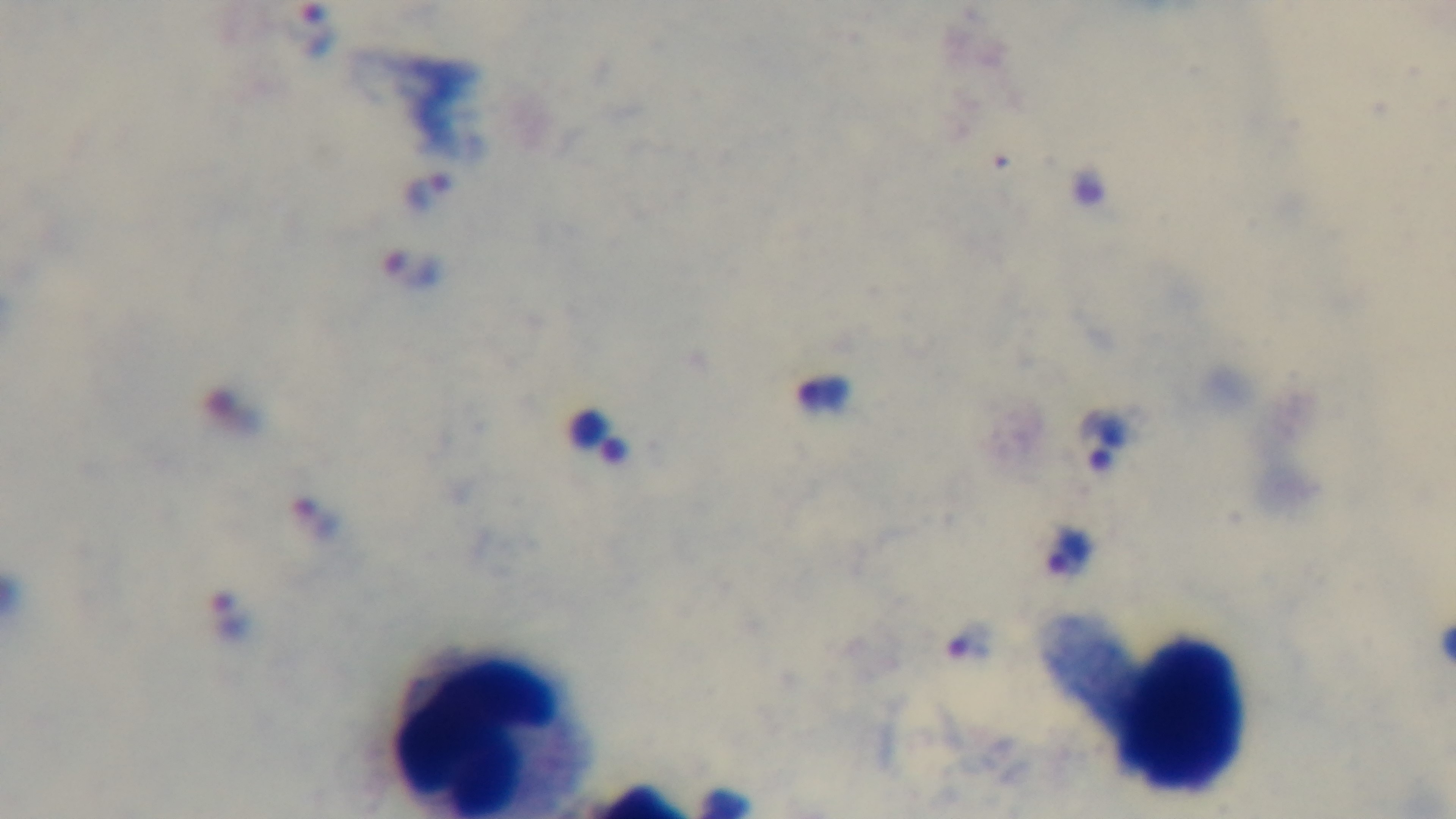

Summary:
  - Preparation: thick
  - Field of view: single
  - Capture: mounted 4K digital camera
  - Modality: light microscopy
  - Objective: 100x oil immersion
  - Stain: Giemsa
  - Malaria status: positive